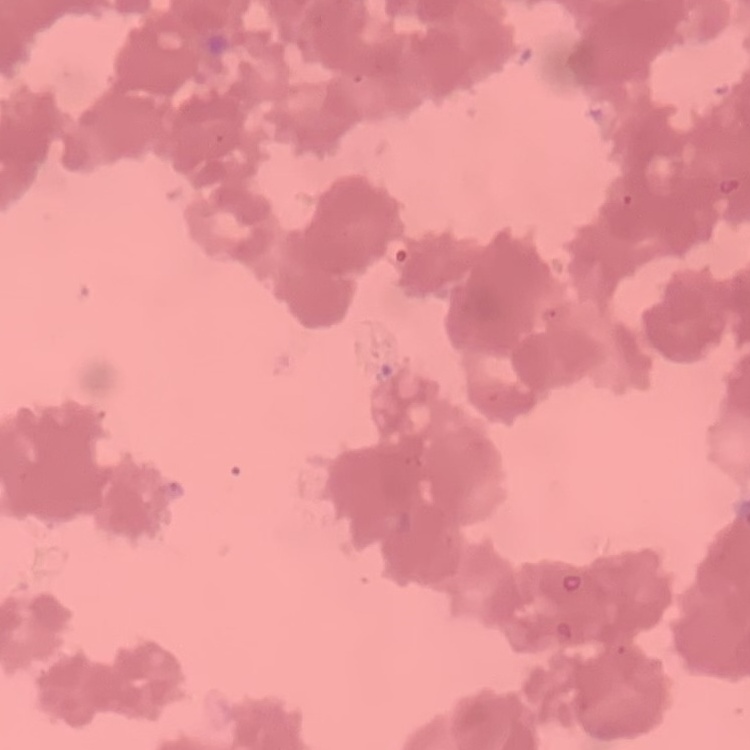

The red blood cells exhibit rouleaux formation. Thin blood film. Square crop of a larger photomicrograph. Stained with either Field's or Giemsa.